Assess the morphology of the erythrocytes.
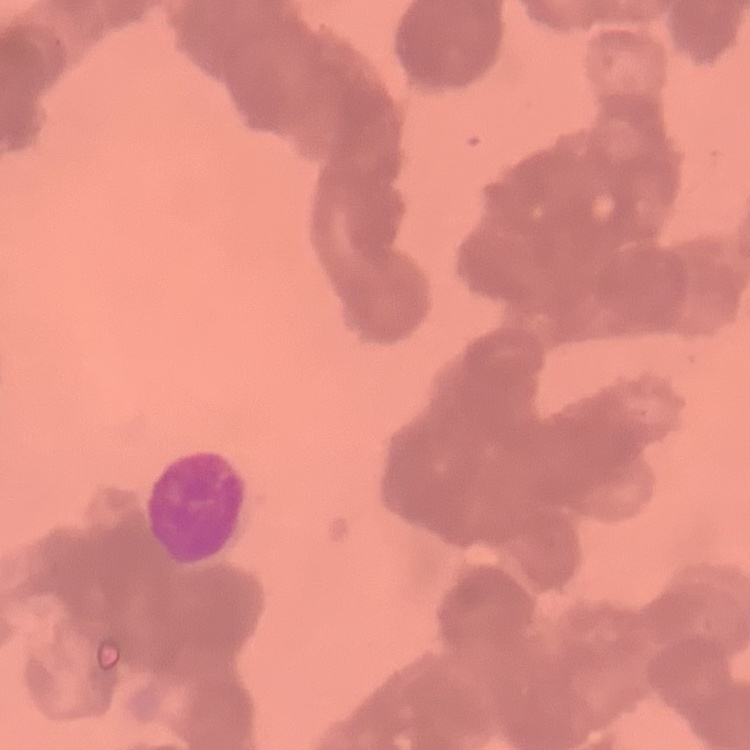

Rouleaux formation.

Thin blood smear. One tile cut from a larger photomicrograph. Field's or Giemsa stain.